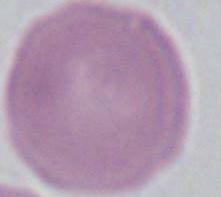

An erythrocyte is seen. Micrograph. Captured at 1000x magnification.